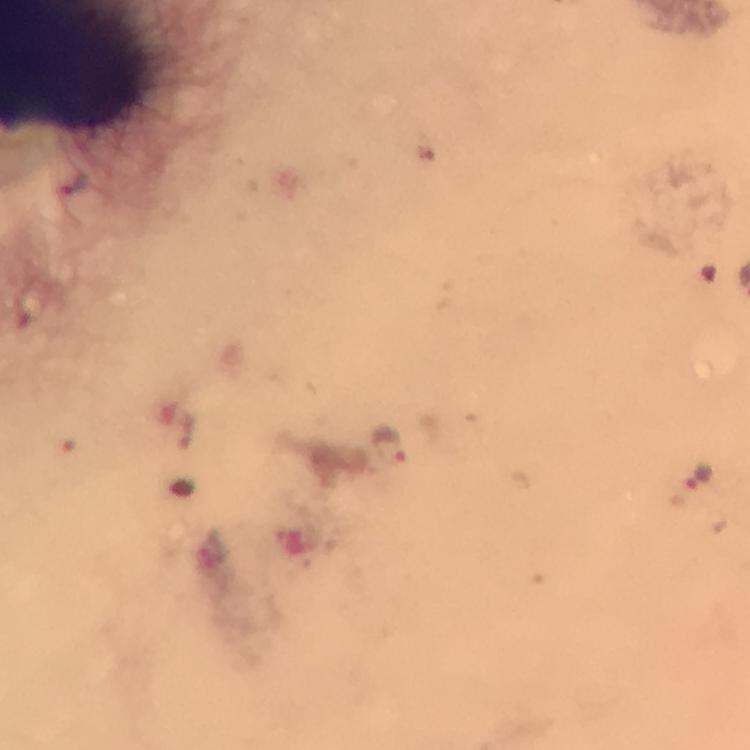

Approximate centers as [x, y] in pixels. Malaria parasite locations: [185, 426], [391, 447], [697, 472]. Cropped region of a single field of view. Immersion oil was used. Giemsa-stained preparation. Smartphone photograph taken through a microscope. Thick smear. Image is 750×750 pixels. At 100x magnification. From a diagnostic examination for malaria.